Locate every Plasmodium parasite.
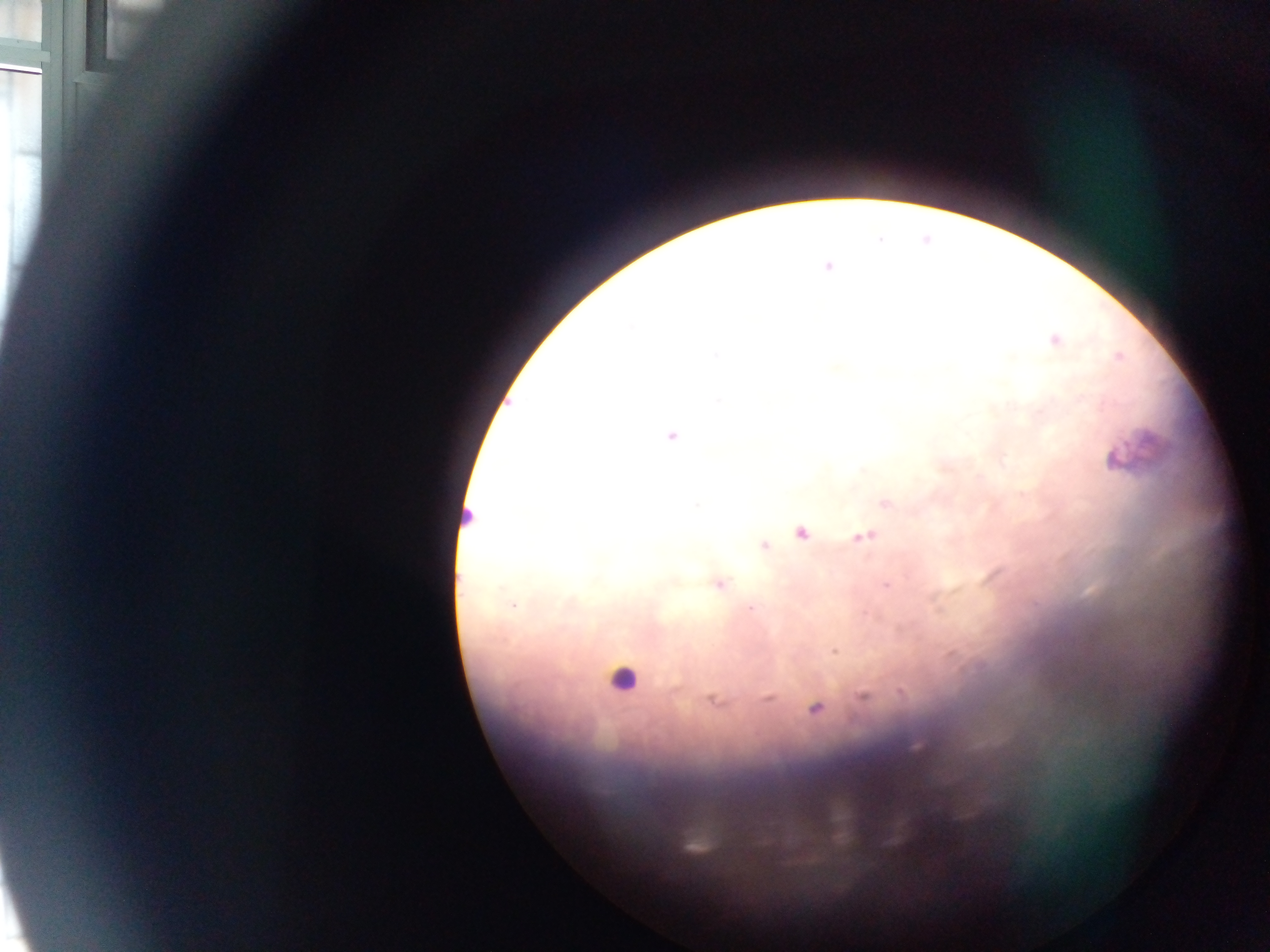

Approximate centers as {x, y} in pixels.
Plasmodium parasites: {828, 267}, {1054, 340}, {716, 355}, {1119, 356}, {1081, 399}, {671, 436}, {1115, 460}, {886, 504}, {801, 532}, {863, 536}, {763, 546}, {719, 585}, {885, 586}, {512, 605}, {750, 608}, {834, 651}, {863, 697}, {767, 698}, {714, 701}, {815, 708}.

Leukocyte locations: {466, 518}, {623, 678}. Thick blood smear. Image is 1270×952 pixels. Single field of view. Photographed through a microscope with a mobile-phone camera. Sample from Ghana.